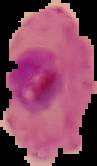
Segmented cell region on a black background. Image is 97×166 pixels. From a thin blood film. Result: malaria parasites identified.